State which parasite is depicted.
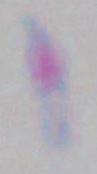
This is Toxoplasma gondii.

Micrograph. Captured at 1000x magnification.